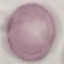
result: no malaria parasites detected
preparation: thin blood smear
stain: Giemsa
capture: smartphone through the microscope eyepiece
image_type: automatically extracted cell patch, resized to 64 × 64 pixels